Report the malaria status of this cell.
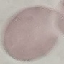
It is uninfected.

Summary:
  - Capture: smartphone camera at the microscope eyepiece
  - Preparation: thin smear
  - Image type: cell patch, automatically extracted from a larger field of view and resized to 64 × 64 pixels
  - Stain: Giemsa